Classify this cell by malaria status.
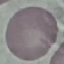
It is uninfected.

Summary:
  - Stain: Giemsa
  - Image type: automatically extracted cell patch, resized to 64 × 64 pixels
  - Capture: smartphone camera at the microscope eyepiece
  - Preparation: thin blood film